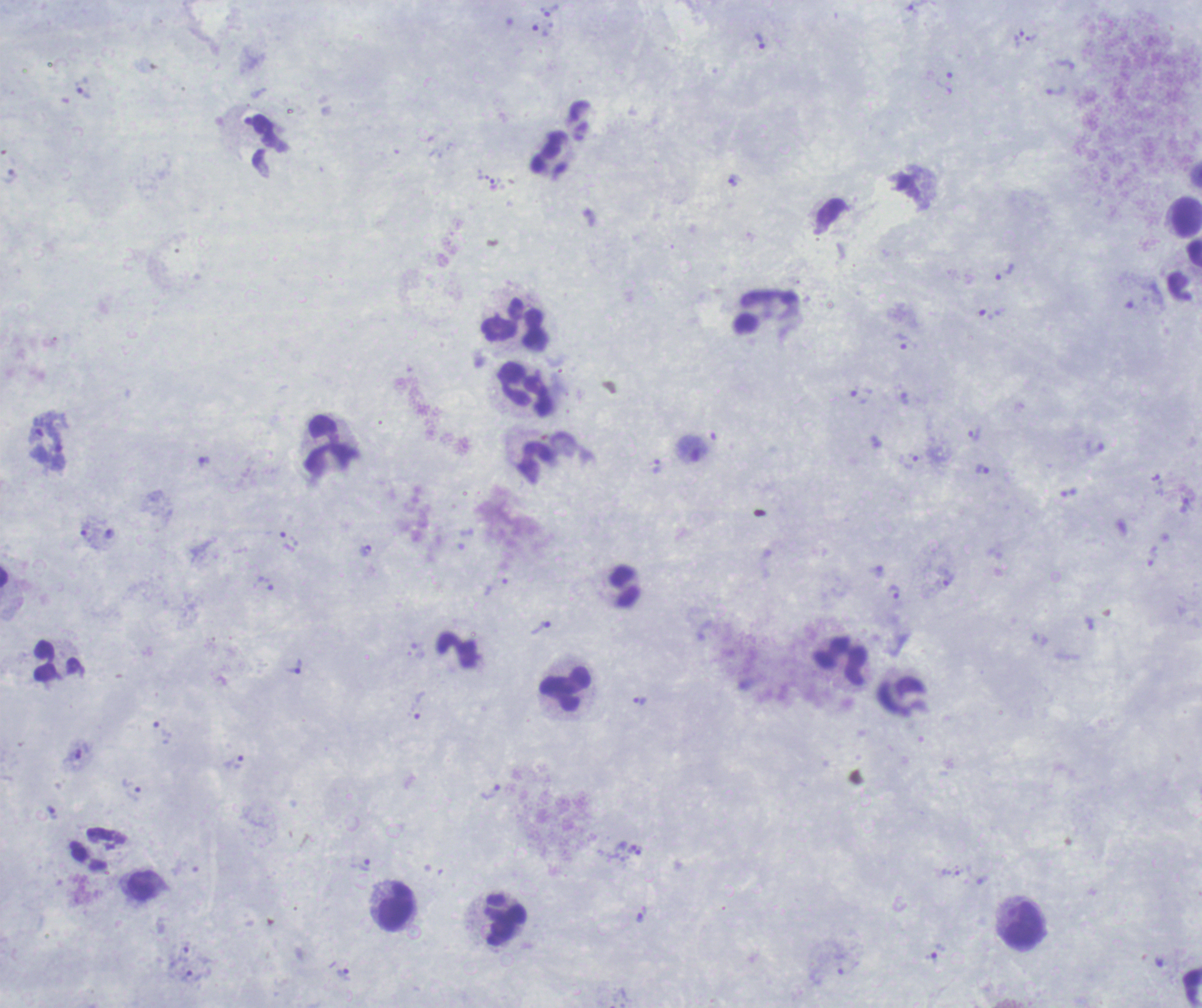
Thick blood smear. Romanowsky-stained preparation. One field from this slide. Image is 1202×1008 pixels.